Report the malaria status of this cell.
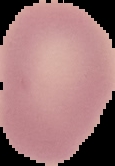
Uninfected.

Summary:
  - Image size: 115×166 pixels
  - Preparation: thin blood smear
  - Image type: segmented cell region on a black background